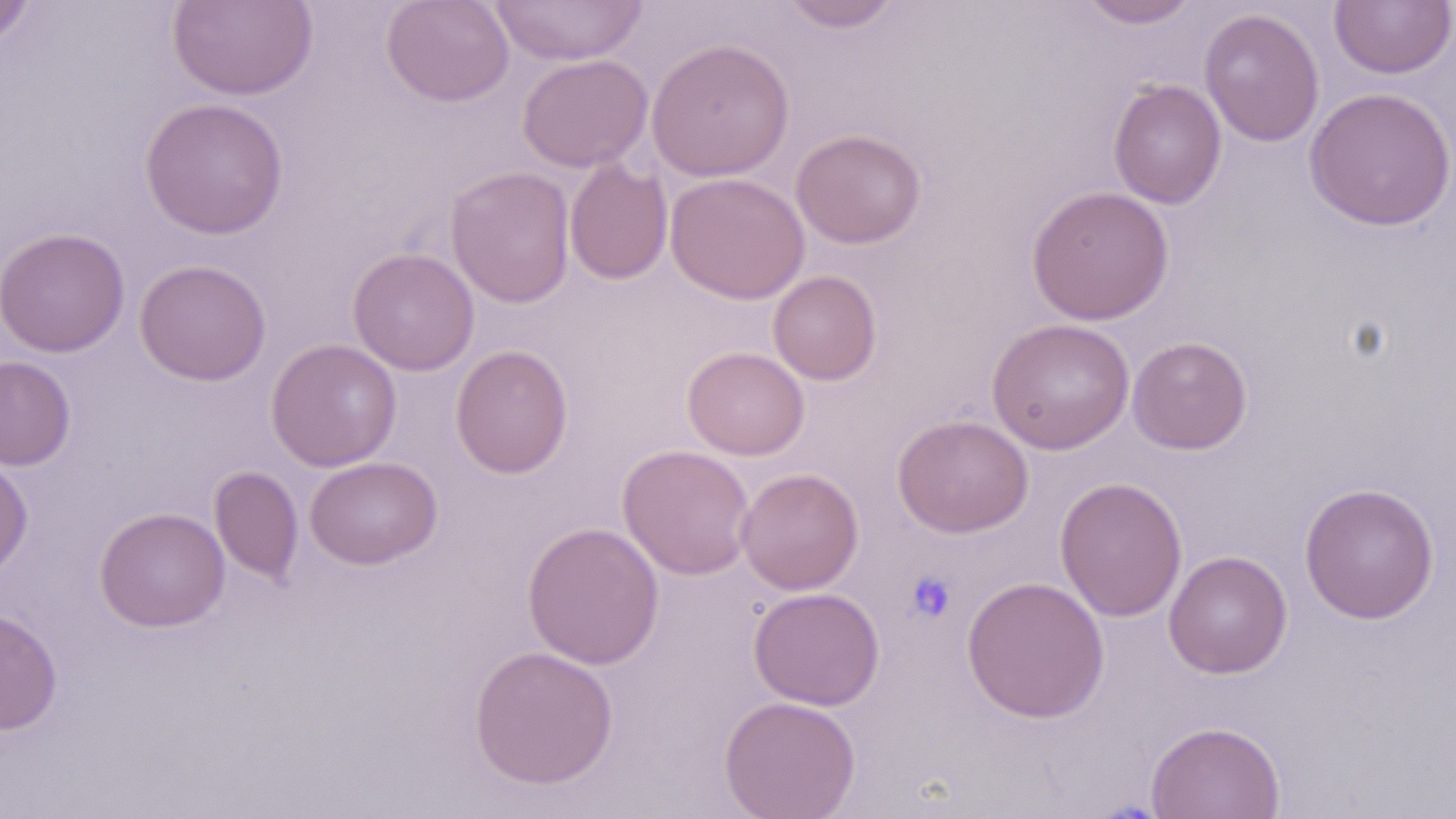

slide-level diagnosis = negative for blood parasites
modality = optical microscopy
image size = 1456×819 pixels
preparation = thin blood smear
uninfected red blood cell locations = approximate bounding boxes as (x1,y1)-(x2,y2) corner pairs in pixels: (165,0)-(318,101), (381,0)-(515,107), (487,0)-(649,66), (780,0)-(902,32), (1079,0)-(1199,29), (1329,0)-(1456,79), (0,1)-(36,52), (1199,7)-(1325,146), (646,38)-(795,181), (517,53)-(653,173), (1108,79)-(1227,209), (1304,87)-(1455,231), (139,97)-(289,239), (790,128)-(927,249), (564,160)-(673,285), (445,166)-(576,308), (665,172)-(810,304), (1026,185)-(1175,325), (0,227)-(130,358), (348,248)-(480,376), (135,258)-(272,385), (767,269)-(882,385), (986,318)-(1135,455), (1127,335)-(1253,454), (266,338)-(402,472), (450,344)-(573,479), (682,346)-(810,461), (0,356)-(76,470), (893,414)-(1033,538), (617,444)-(756,580), (0,455)-(33,580), (305,456)-(442,570), (210,466)-(305,586), (736,467)-(864,595), (1055,476)-(1187,622), (1299,481)-(1439,624), (94,506)-(230,633), (522,521)-(665,670), (1163,550)-(1292,679), (960,575)-(1110,722), (748,587)-(885,710), (0,607)-(63,735), (469,645)-(619,790), (719,695)-(861,818), (1145,720)-(1286,819)
magnification = 1000x
platelet locations = approximate bounding boxes as (x1,y1)-(x2,y2) corner pairs in pixels: (905,569)-(958,622)
stain = May-Grünwald-Giemsa
field of view = one of a larger specimen